Classify this cell by malaria status.
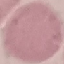
It is uninfected.

preparation: thin smear
stain: Giemsa
capture: smartphone camera at the microscope eyepiece
image_type: cell patch, automatically extracted from a larger field of view and resized to 64 × 64 pixels